Locate Plasmodium parasites and white blood cells.
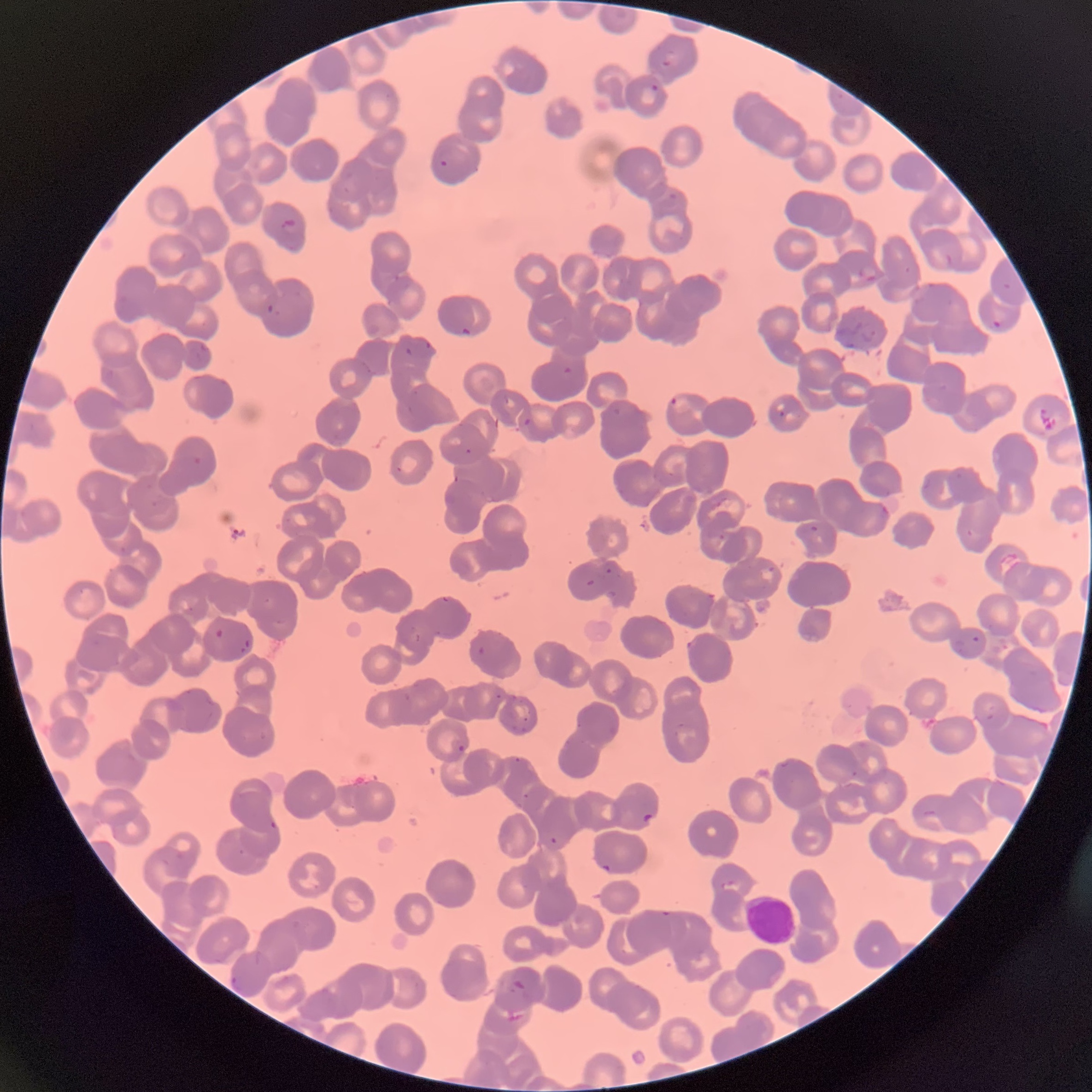
Approximate bounding boxes as [x1, y1, x2, y2] in pixels.
Plasmodium parasites: [662, 48, 675, 68], [650, 83, 659, 93], [440, 159, 449, 167], [669, 192, 677, 199], [278, 218, 298, 233], [859, 265, 877, 282], [1001, 283, 1012, 291], [266, 304, 281, 318], [992, 320, 1003, 328], [462, 327, 472, 337], [861, 329, 877, 342], [404, 346, 414, 355], [563, 366, 573, 375], [669, 396, 694, 413], [779, 409, 786, 417], [523, 417, 532, 425], [193, 457, 203, 465], [395, 465, 403, 473], [810, 525, 819, 532], [585, 579, 596, 586], [215, 628, 224, 639], [952, 639, 966, 654], [478, 645, 487, 655], [457, 743, 467, 753], [515, 756, 526, 763], [643, 813, 654, 824], [270, 820, 278, 829], [601, 863, 614, 873], [722, 880, 742, 893], [659, 910, 672, 918], [230, 975, 241, 991], [512, 977, 530, 994].
Plasmodium parasites too small for a box (approximate centers as [x, y] in pixels): [468, 451], [456, 479], [608, 571], [498, 697], [554, 840].
White blood cells: [745, 895, 796, 945].

preparation = thin blood film
modality = optical microscopy
image size = 1092×1092 pixels
red blood cell morphology = rouleaux formation